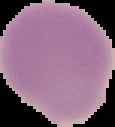
Summary:
  - Image type: cell region segmented out of the field of view; surrounding area masked to black
  - Result: no Plasmodium parasites detected
  - Preparation: thin blood film
  - Image size: 115×127 pixels